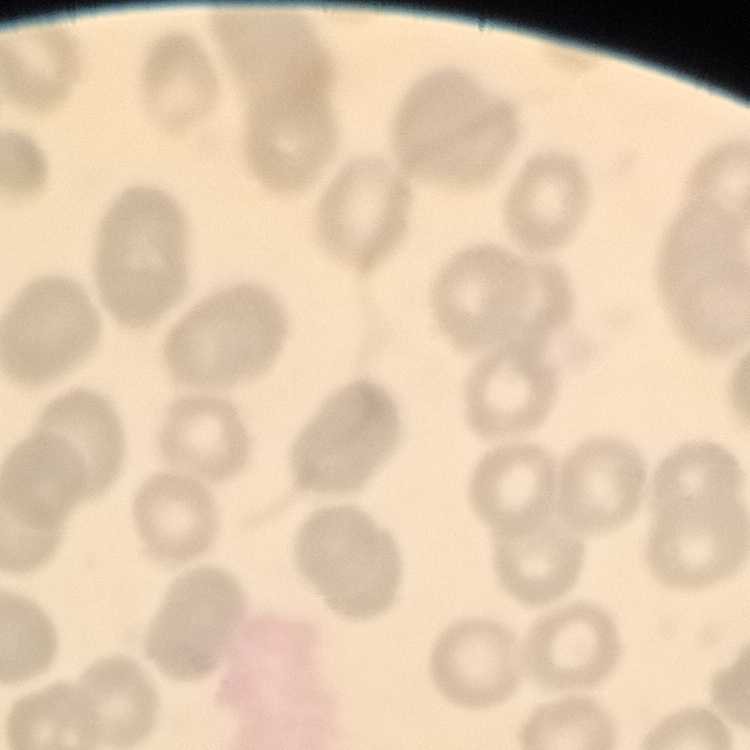
{
  "red_blood_cell_morphology": "no rouleaux formation",
  "stain": "Field's or Giemsa",
  "preparation": "thin blood film",
  "image_type": "square crop of a larger photomicrograph"
}